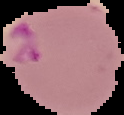

Summary:
  - Image type: cell region segmented out of the field of view; surrounding area masked to black
  - Image size: 124×115 pixels
  - Malaria status: parasitized
  - Preparation: thin blood film